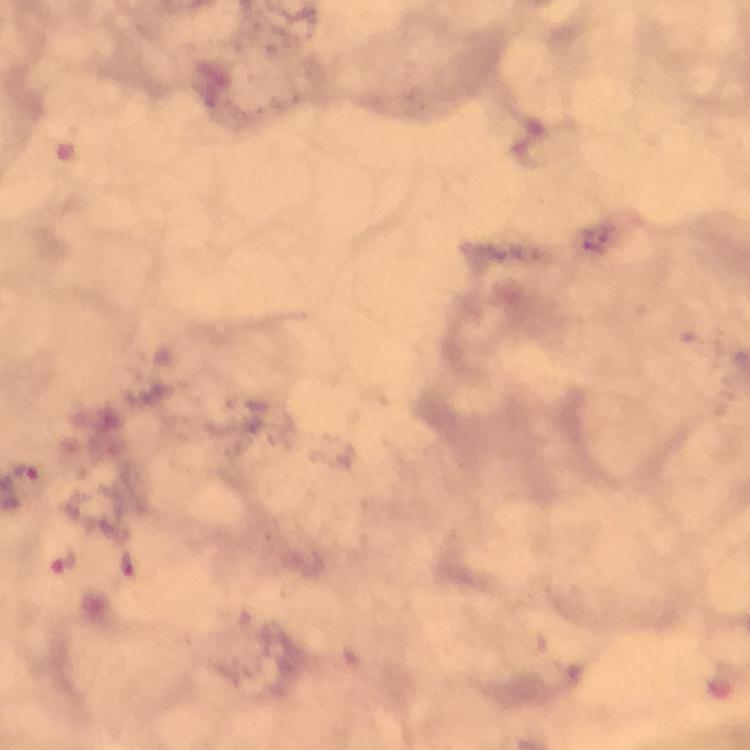

Approximate centers as (x, y) in pixels. Plasmodium parasite locations: (25, 471), (64, 559). Thick smear. Giemsa stain. Cropped region of a single field of view. From a malaria diagnostic workup. Photographed with a smartphone mounted on the microscope. 100x magnification. Image is 750×750 pixels. Immersion oil applied.